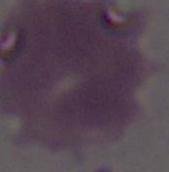

Summary:
  - Magnification: 1000x
  - Identification: red blood cell
  - Modality: photomicrograph